Identify the parasite.
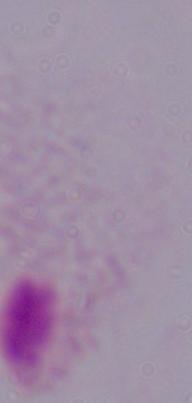

A trichomonad.

Summary:
  - Magnification: 1000x
  - Modality: photomicrograph